Report the malaria status of this cell.
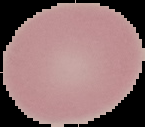
Uninfected.

From a thin blood film. The area outside the segmented cell region is set to black. Image is 145×127 pixels.